Name the parasite shown.
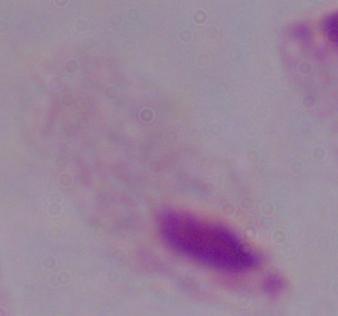

A trichomonad.

1000x magnification. Micrograph.